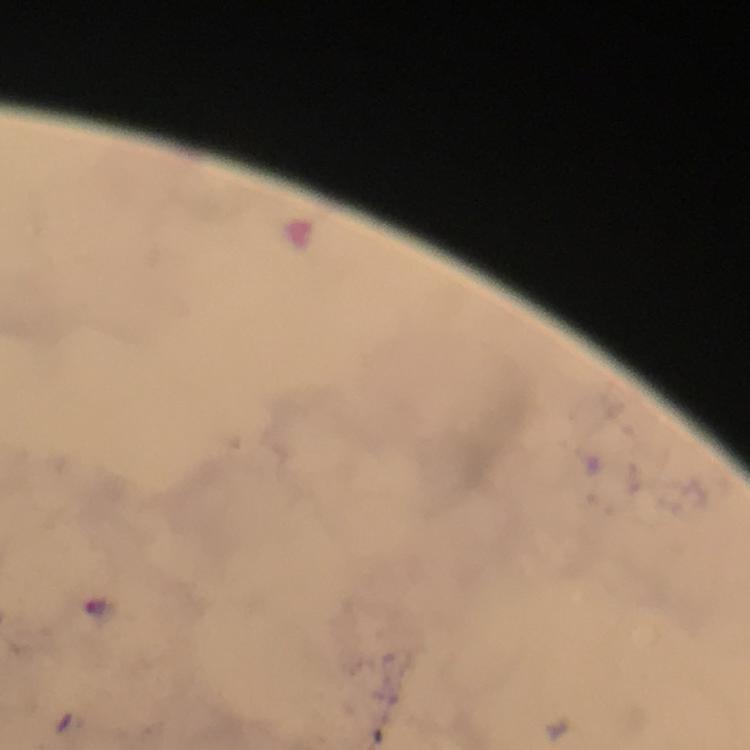

stain: Giemsa
preparation: thick blood film
plasmodium_parasite_locations: 'approximate object centers, in pixels from the top-left corner: (x=98, y=609)'
immersion_oil: used
capture: smartphone photograph through a microscope
context: from a diagnostic examination for malaria
image_size: 750×750 pixels
cropped_from: one field of view
magnification: 100x